Locate every Plasmodium falciparum-infected red blood cell.
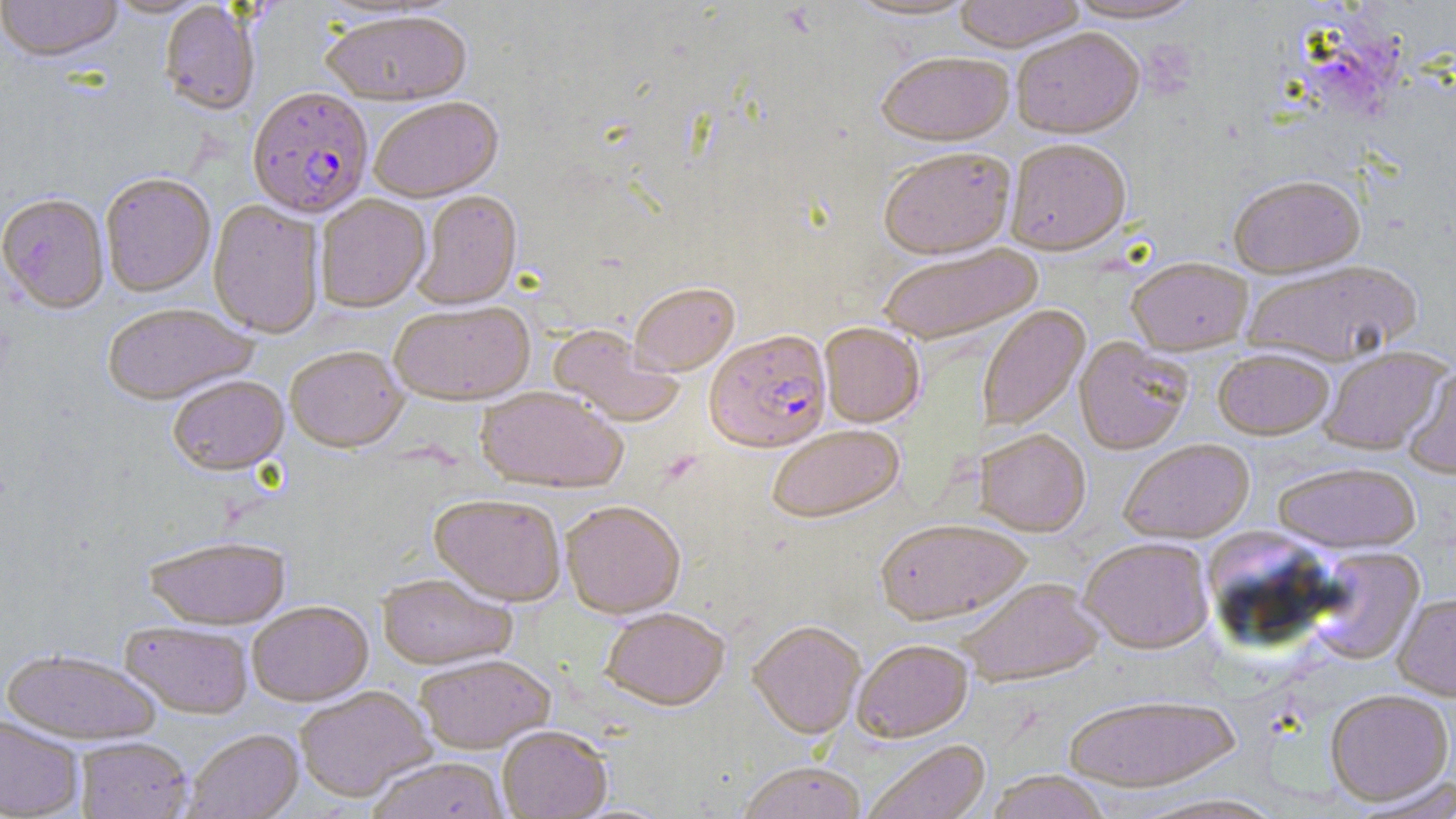

Approximate bounding boxes as [x1, y1, x2, y2] in pixels.
Plasmodium falciparum-infected red blood cells: [248, 85, 374, 217], [705, 329, 831, 451].

Summary:
  - Uninfected red blood cell locations: [0, 0, 123, 61], [102, 0, 211, 18], [843, 0, 982, 22], [952, 0, 1086, 51], [1062, 0, 1207, 24], [159, 1, 260, 115], [320, 8, 472, 105], [1011, 26, 1144, 138], [876, 49, 1014, 144], [368, 96, 503, 201], [1005, 137, 1131, 254], [878, 145, 1015, 258], [100, 171, 216, 296], [1227, 173, 1365, 277], [413, 189, 522, 308], [0, 192, 110, 312], [315, 194, 430, 312], [208, 199, 325, 338], [876, 243, 1043, 344], [1126, 256, 1253, 354], [1240, 259, 1423, 366], [629, 281, 739, 374], [389, 299, 535, 404], [101, 302, 257, 403], [977, 305, 1089, 431], [820, 322, 924, 426], [547, 324, 685, 426], [1074, 337, 1193, 454], [285, 344, 408, 451], [1319, 346, 1449, 454], [1213, 348, 1334, 439], [1402, 362, 1456, 480], [167, 373, 288, 474], [476, 386, 628, 492], [766, 423, 904, 522], [975, 428, 1091, 535], [1119, 438, 1254, 542], [1271, 461, 1422, 552], [430, 492, 567, 605], [560, 499, 685, 617], [875, 517, 1032, 624], [1201, 527, 1337, 642], [143, 535, 291, 629], [1079, 537, 1214, 652], [1306, 547, 1424, 665], [377, 572, 517, 669], [958, 577, 1104, 685], [1392, 593, 1456, 701], [247, 600, 373, 706], [601, 606, 730, 709], [749, 619, 866, 737], [120, 621, 254, 718], [852, 639, 973, 741], [2, 647, 163, 744], [414, 653, 555, 753], [294, 685, 436, 803], [1324, 688, 1454, 805], [1062, 692, 1242, 791], [0, 714, 84, 818], [497, 724, 612, 818], [184, 728, 303, 818], [75, 736, 193, 819], [863, 739, 991, 819], [367, 756, 510, 819], [737, 761, 867, 819], [984, 770, 1112, 819], [1355, 776, 1456, 817], [1126, 792, 1288, 818]
  - Slide-level diagnosis: Plasmodium falciparum
  - Image size: 1456×819 pixels
  - Magnification: 1000x
  - Modality: light microscopy
  - Field of view: single
  - Stain: May-Grünwald-Giemsa
  - Preparation: thin blood smear